Report the malaria status of this cell.
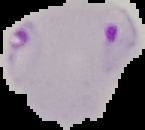
It is parasitized.

preparation = thin blood smear
image type = segmented cell region with the area outside set to black
image size = 145×130 pixels